Report the malaria status.
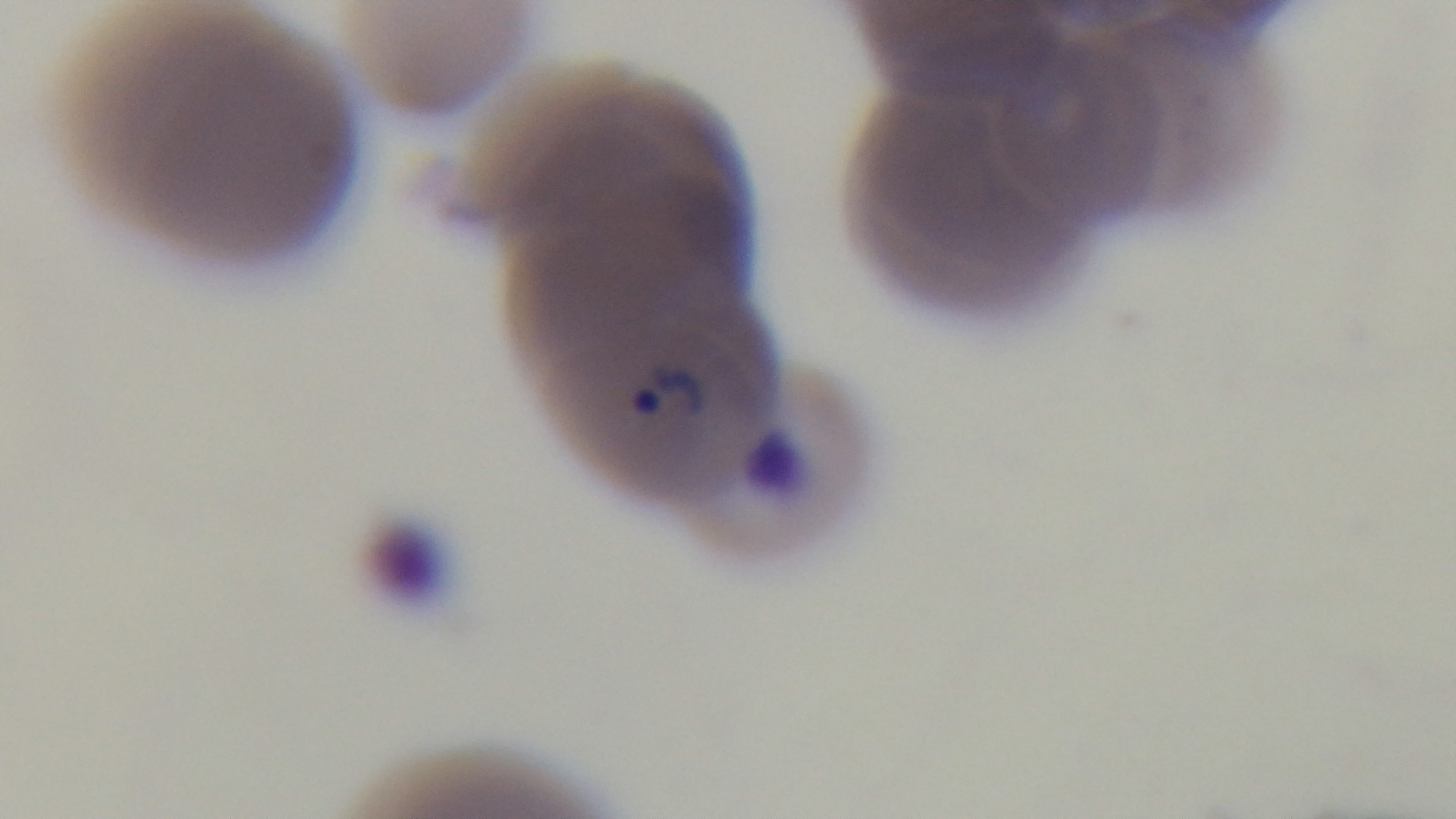

It is infected.

preparation = thin smear
stain = Giemsa
objective = 100x oil immersion
capture = mounted 4K digital camera
modality = light microscopy
field of view = one from the slide